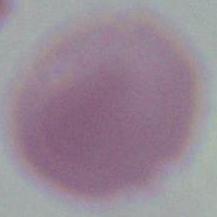

modality = micrograph
identification = red blood cell
magnification = 1000x